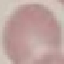

Malaria status: uninfected. Thin blood smear. Cell patch, automatically extracted from a larger field of view and resized to 64 × 64 pixels. Acquired by smartphone through the microscope eyepiece. Giemsa-stained preparation.